Classify this cell by malaria status.
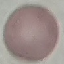
It is uninfected.

Giemsa-stained preparation. Photographed with a smartphone camera at the microscope eyepiece. Automatically extracted cell patch, resized to 64 × 64 pixels. Thin blood film.